Report the malaria status of this cell.
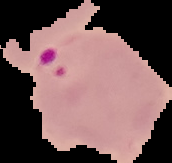
It is parasitized.

Summary:
  - Image size: 172×163 pixels
  - Image type: cell region segmented out of the field of view; surrounding area masked to black
  - Preparation: thin blood film